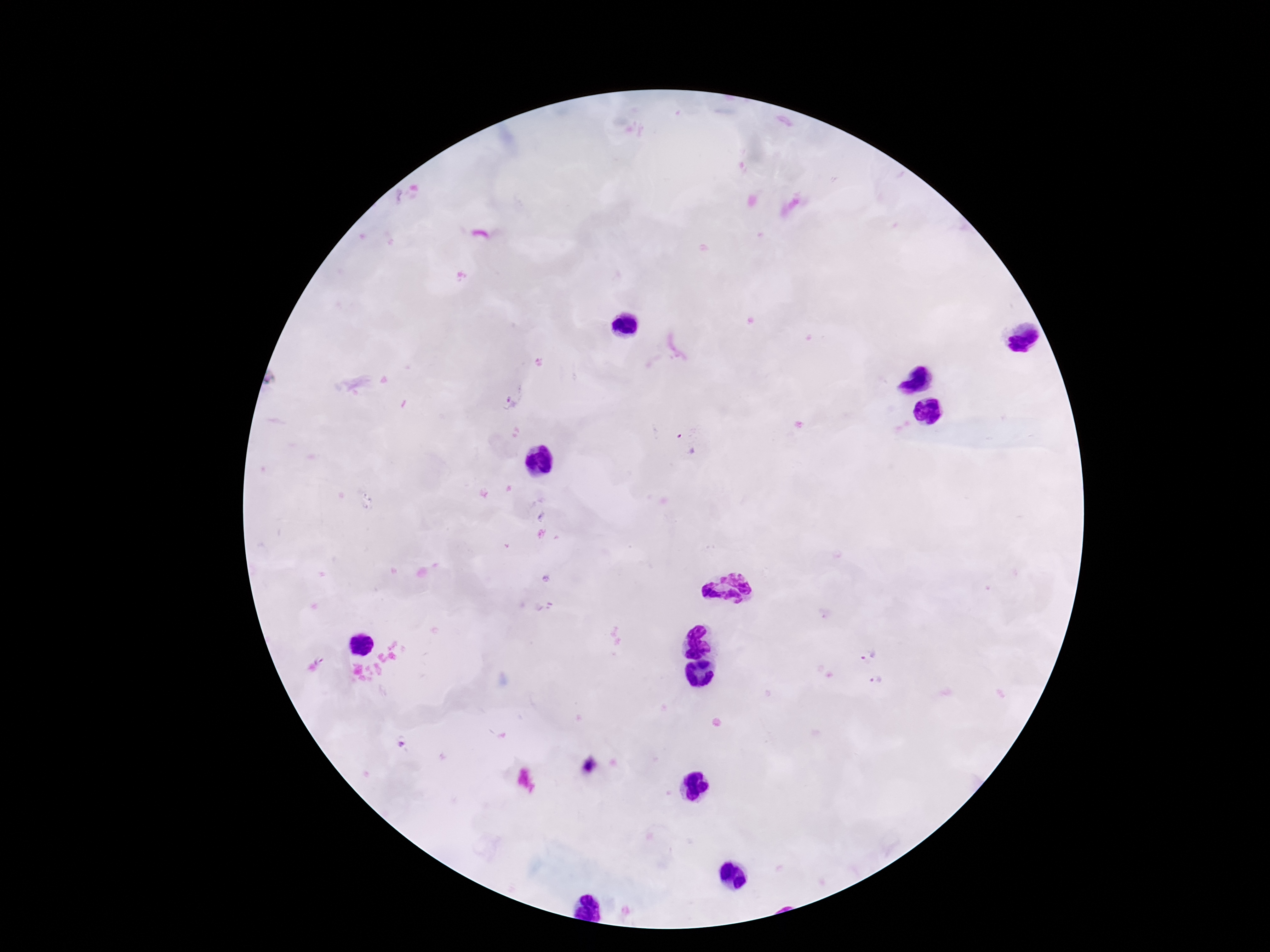

Approximate centers as [x, y] in pixels.
Summary:
  - Plasmodium parasite locations: [512, 396], [685, 444], [869, 652], [877, 680]
  - Patient malaria status: positive
  - Preparation: thick peripheral-blood smear
  - Image size: 1270×952 pixels
  - Stain: Giemsa
  - Field of view: one from this slide
  - Magnification: 100x
  - Capture: smartphone camera through the microscope eyepiece